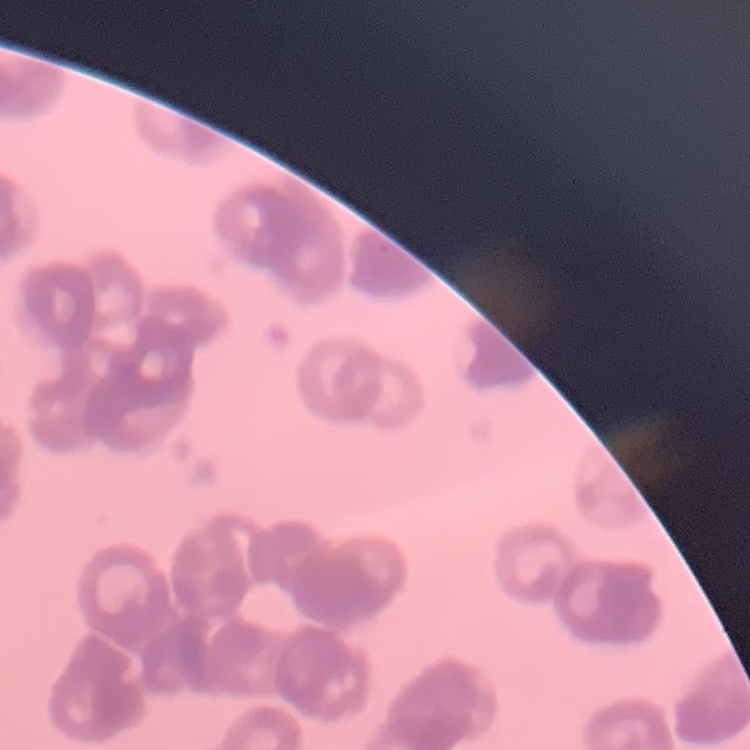

{
  "red_blood_cell_morphology": "rouleaux formation",
  "image_type": "one tile cut from a larger photomicrograph",
  "stain": "Field's or Giemsa",
  "preparation": "thin blood smear"
}